Describe the morphology of the red blood cells.
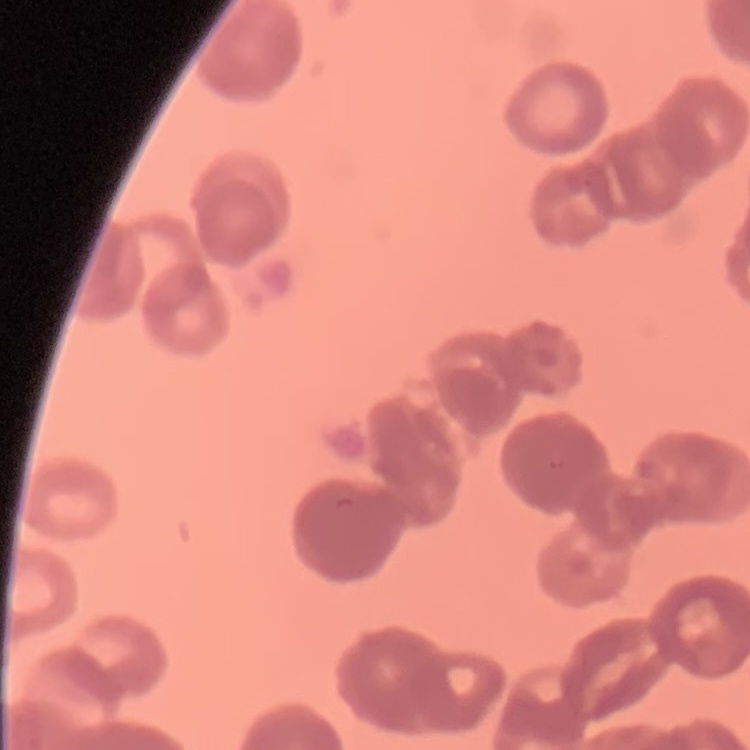
They show rouleaux formation.

preparation = thin peripheral smear
image type = square crop of a larger photomicrograph
stain = Field's or Giemsa